Report the malaria status of this cell.
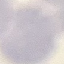

Uninfected.

preparation = thin blood film
capture = smartphone camera at the microscope eyepiece
stain = Giemsa
image type = automatically extracted cell patch, resized to 64 × 64 pixels